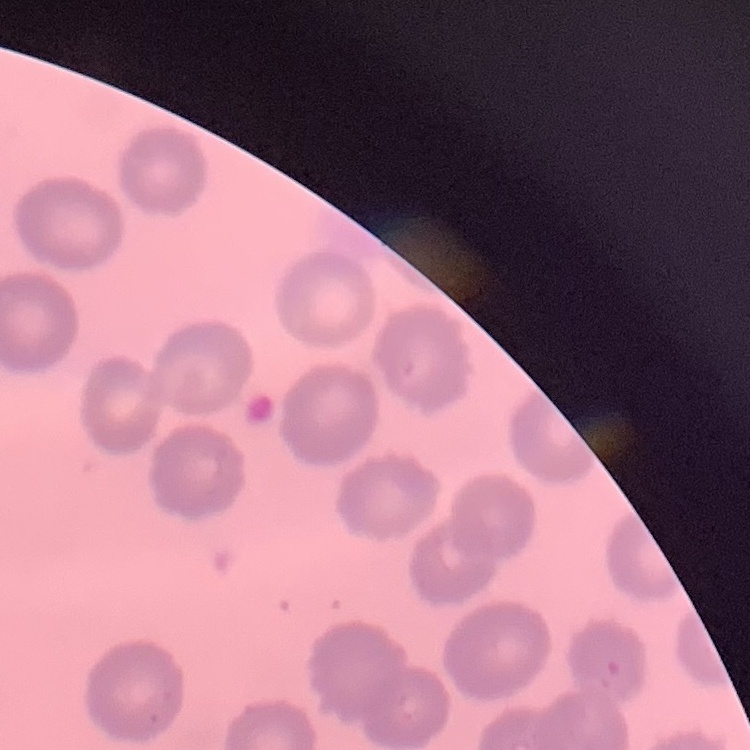
Summary:
  - Erythrocyte morphology: no rouleaux formation
  - Preparation: thin peripheral smear
  - Stain: Field's or Giemsa
  - Image type: square crop of a larger photomicrograph